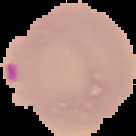
malaria status = parasitized
image size = 136×136 pixels
preparation = thin blood smear
image type = segmented cell region on a black background